State the blood parasite species.
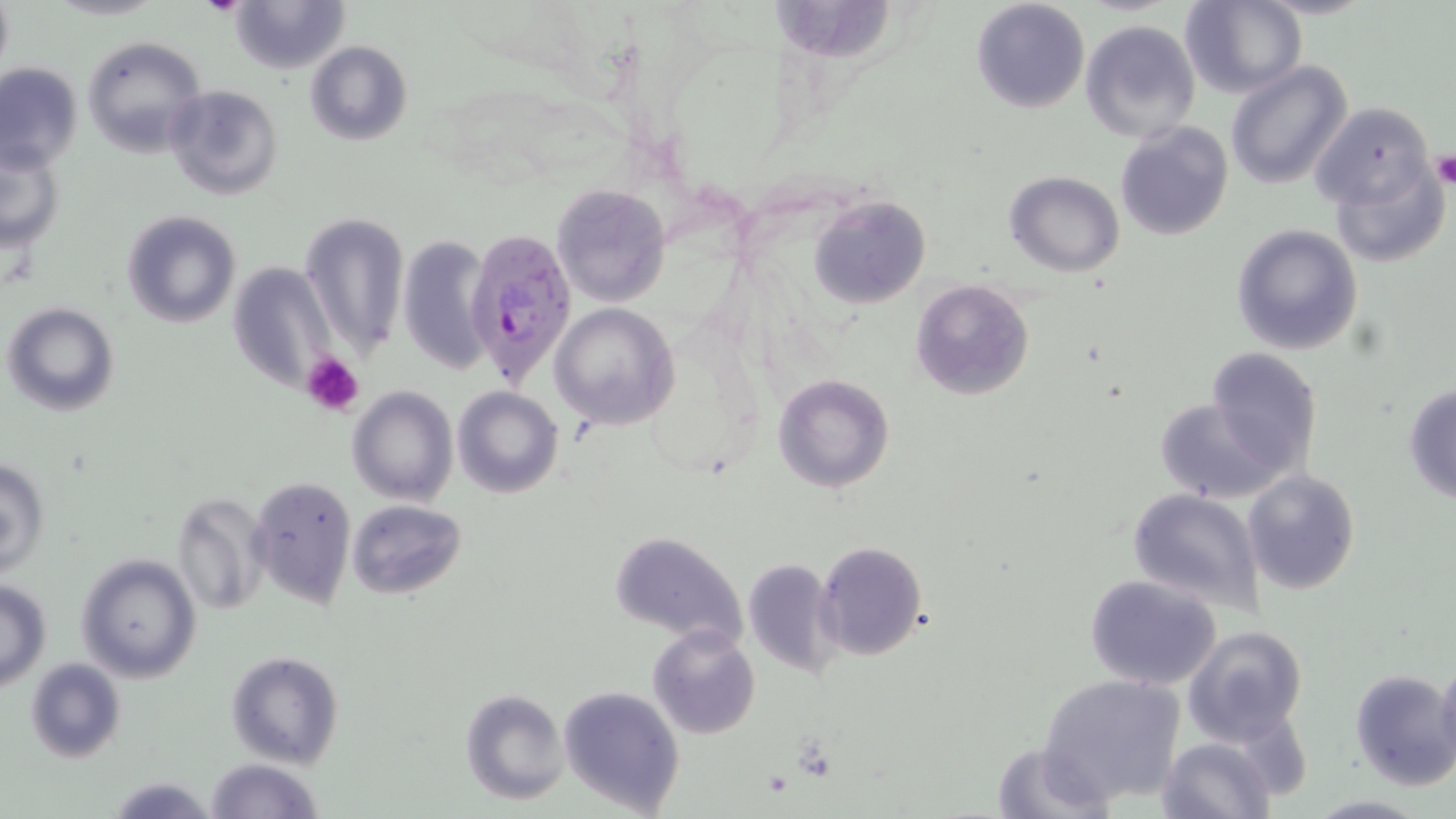

Plasmodium falciparum.

Summary:
  - Coordinate format: approximate bounding boxes as (x1,y1)-(x2,y2) corner pairs in pixels
  - Plasmodium falciparum-infected red blood cell locations: (465,230)-(578,388)
  - Uninfected red blood cell locations: (0,0)-(13,76), (230,0)-(349,73), (971,0)-(1089,112), (1183,0)-(1306,98), (766,1)-(897,62), (1080,19)-(1200,142), (81,36)-(205,156), (304,40)-(412,145), (1226,61)-(1353,191), (0,62)-(82,173), (165,84)-(283,199), (1310,101)-(1439,215), (1115,122)-(1233,241), (0,147)-(64,253), (1328,152)-(1450,269), (1006,172)-(1125,275), (551,183)-(671,309), (807,196)-(931,309), (122,210)-(240,328), (300,213)-(410,359), (1230,223)-(1366,356), (396,235)-(491,375), (229,259)-(337,390), (910,279)-(1035,401), (5,303)-(119,416), (550,303)-(679,429), (1205,346)-(1323,471), (773,373)-(893,493), (1402,381)-(1456,506), (348,384)-(458,506), (451,386)-(564,499), (1152,397)-(1285,503), (1,456)-(49,576), (1242,469)-(1360,594), (247,474)-(357,608), (1126,488)-(1266,610), (172,490)-(272,616), (347,499)-(467,598), (608,531)-(749,650), (816,541)-(927,661), (75,553)-(202,682), (741,557)-(843,678), (1083,574)-(1225,691), (0,580)-(49,690), (647,625)-(760,739), (1182,626)-(1308,746), (225,650)-(344,768), (1437,652)-(1456,771), (25,657)-(125,764), (1350,669)-(1456,790), (1039,673)-(1186,804), (558,684)-(686,816), (460,687)-(571,805), (1158,737)-(1274,819), (990,740)-(1115,818), (203,757)-(325,818), (106,775)-(220,817), (1306,794)-(1429,818)
  - Platelet locations: (199,0)-(249,16), (1430,152)-(1456,188), (302,353)-(366,417)
  - Image size: 1456×819 pixels
  - Stain: May-Grünwald-Giemsa
  - Modality: optical microscopy
  - Preparation: thin blood smear
  - Magnification: 1000x
  - Field of view: single